Name the parasite shown.
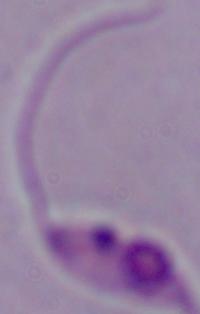

Leishmania.

magnification = 1000x
modality = micrograph